State the blood parasite species.
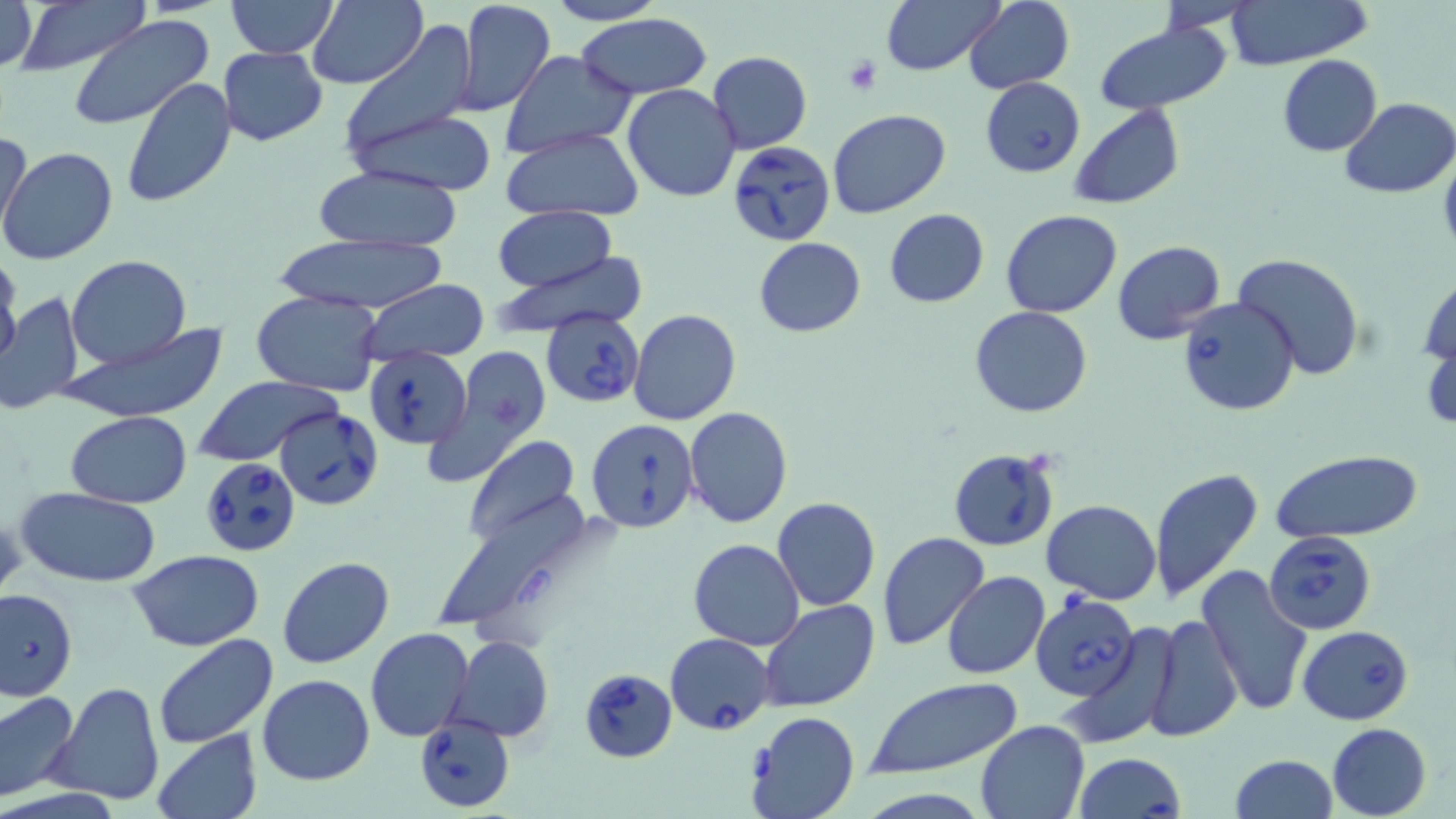

Babesia divergens.

field of view = single
preparation = thin blood smear
stain = May-Grünwald-Giemsa
magnification = 1000x
modality = light microscopy
platelet locations = approximate bounding boxes as named x1/y1/x2/y2 corners in pixels: (x1=841, y1=56, x2=881, y2=96)
uninfected red blood cell locations = approximate bounding boxes as named x1/y1/x2/y2 corners in pixels: (x1=0, y1=0, x2=38, y2=72), (x1=9, y1=0, x2=152, y2=75), (x1=225, y1=0, x2=340, y2=59), (x1=308, y1=0, x2=428, y2=91), (x1=453, y1=0, x2=556, y2=118), (x1=545, y1=0, x2=665, y2=26), (x1=880, y1=0, x2=1004, y2=76), (x1=962, y1=0, x2=1075, y2=93), (x1=1150, y1=0, x2=1255, y2=33), (x1=1223, y1=1, x2=1373, y2=70), (x1=576, y1=12, x2=713, y2=99), (x1=67, y1=15, x2=215, y2=132), (x1=338, y1=22, x2=481, y2=155), (x1=1093, y1=22, x2=1233, y2=115), (x1=217, y1=46, x2=328, y2=147), (x1=503, y1=51, x2=638, y2=155), (x1=707, y1=51, x2=812, y2=154), (x1=1277, y1=54, x2=1383, y2=155), (x1=120, y1=76, x2=234, y2=208), (x1=622, y1=84, x2=741, y2=202), (x1=1340, y1=98, x2=1456, y2=197), (x1=1067, y1=104, x2=1186, y2=210), (x1=350, y1=107, x2=497, y2=195), (x1=828, y1=107, x2=949, y2=218), (x1=1, y1=126, x2=32, y2=243), (x1=500, y1=128, x2=645, y2=221), (x1=1, y1=146, x2=118, y2=265), (x1=313, y1=164, x2=463, y2=252), (x1=492, y1=206, x2=618, y2=292), (x1=884, y1=208, x2=989, y2=308), (x1=1000, y1=210, x2=1123, y2=318), (x1=267, y1=234, x2=456, y2=315), (x1=753, y1=237, x2=867, y2=337), (x1=1113, y1=240, x2=1226, y2=347), (x1=1232, y1=252, x2=1365, y2=380), (x1=0, y1=253, x2=23, y2=371), (x1=491, y1=253, x2=649, y2=336), (x1=67, y1=255, x2=192, y2=370), (x1=1418, y1=267, x2=1455, y2=374), (x1=359, y1=280, x2=489, y2=365), (x1=252, y1=289, x2=382, y2=396), (x1=0, y1=290, x2=85, y2=416), (x1=970, y1=306, x2=1093, y2=417), (x1=629, y1=309, x2=740, y2=426), (x1=62, y1=325, x2=228, y2=420), (x1=1423, y1=325, x2=1455, y2=440), (x1=423, y1=347, x2=551, y2=486), (x1=195, y1=375, x2=343, y2=467), (x1=683, y1=407, x2=793, y2=529), (x1=65, y1=410, x2=191, y2=508), (x1=463, y1=435, x2=581, y2=547), (x1=1269, y1=448, x2=1426, y2=545), (x1=1149, y1=466, x2=1265, y2=605), (x1=16, y1=487, x2=162, y2=588), (x1=430, y1=493, x2=607, y2=642), (x1=772, y1=497, x2=880, y2=611), (x1=1041, y1=499, x2=1162, y2=603), (x1=0, y1=505, x2=25, y2=608), (x1=877, y1=531, x2=990, y2=650), (x1=689, y1=538, x2=805, y2=650), (x1=129, y1=550, x2=263, y2=651), (x1=278, y1=557, x2=395, y2=669), (x1=1196, y1=564, x2=1313, y2=716), (x1=940, y1=572, x2=1050, y2=678), (x1=759, y1=600, x2=879, y2=714), (x1=1143, y1=613, x2=1243, y2=741), (x1=365, y1=627, x2=474, y2=742), (x1=1058, y1=633, x2=1178, y2=751), (x1=151, y1=634, x2=277, y2=750), (x1=450, y1=636, x2=552, y2=742), (x1=258, y1=673, x2=375, y2=786), (x1=864, y1=677, x2=1024, y2=782), (x1=45, y1=682, x2=165, y2=806), (x1=0, y1=689, x2=79, y2=801), (x1=744, y1=711, x2=859, y2=819), (x1=974, y1=718, x2=1089, y2=819), (x1=1327, y1=722, x2=1431, y2=818), (x1=152, y1=730, x2=261, y2=818), (x1=1229, y1=755, x2=1339, y2=819)
image size = 1456×819 pixels
Babesia divergens-infected red blood cell locations = approximate bounding boxes as named x1/y1/x2/y2 corners in pixels: (x1=980, y1=76, x2=1085, y2=176), (x1=728, y1=141, x2=836, y2=246), (x1=1175, y1=297, x2=1300, y2=418), (x1=542, y1=311, x2=644, y2=407), (x1=365, y1=347, x2=470, y2=448), (x1=276, y1=406, x2=385, y2=512), (x1=586, y1=418, x2=700, y2=533), (x1=948, y1=448, x2=1061, y2=552), (x1=199, y1=456, x2=303, y2=558), (x1=1264, y1=529, x2=1378, y2=635), (x1=0, y1=587, x2=78, y2=702), (x1=1032, y1=595, x2=1141, y2=699), (x1=1297, y1=625, x2=1415, y2=725), (x1=666, y1=633, x2=774, y2=735), (x1=582, y1=666, x2=679, y2=762), (x1=414, y1=717, x2=514, y2=812), (x1=1073, y1=752, x2=1187, y2=819)